Locate every Plasmodium falciparum-infected red blood cell.
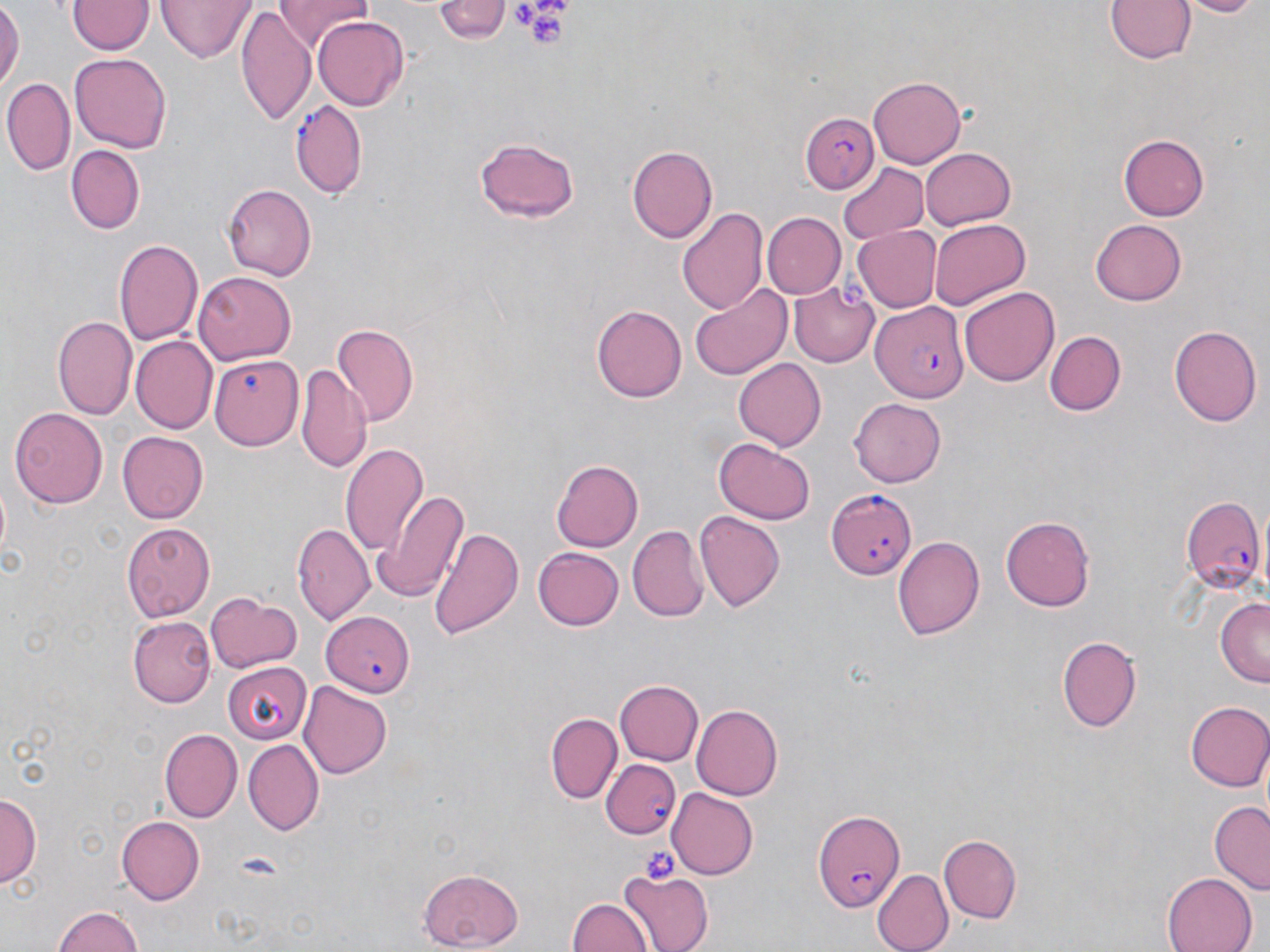
Approximate bounding boxes as (x1,y1)-(x2,y2) corner pairs in pixels.
Plasmodium falciparum-infected red blood cells: (291,99)-(367,198), (801,112)-(877,193), (869,300)-(966,407), (825,487)-(916,578), (1181,495)-(1266,592), (322,609)-(414,698), (601,760)-(681,839), (810,805)-(908,911).

Summary:
  - Uninfected red blood cell locations: (0,0)-(22,92), (158,0)-(255,63), (278,0)-(374,47), (432,0)-(511,43), (1105,0)-(1196,67), (1174,0)-(1264,17), (69,1)-(151,56), (236,8)-(313,124), (311,16)-(409,111), (70,53)-(172,152), (865,75)-(966,169), (4,79)-(75,173), (1120,134)-(1211,221), (476,135)-(581,224), (626,143)-(717,241), (66,145)-(146,233), (920,147)-(1018,230), (837,162)-(928,242), (222,183)-(314,279), (677,205)-(769,316), (761,213)-(844,298), (929,219)-(1030,311), (1089,219)-(1186,306), (853,226)-(940,311), (115,237)-(205,346), (194,270)-(297,362), (789,284)-(878,366), (690,285)-(793,379), (959,287)-(1059,386), (592,304)-(687,403), (52,315)-(137,421), (330,325)-(417,426), (1169,325)-(1261,428), (1044,330)-(1126,416), (131,335)-(218,432), (209,354)-(304,452), (735,358)-(828,450), (297,365)-(372,475), (849,397)-(948,486), (9,408)-(107,508), (117,430)-(209,521), (715,438)-(814,524), (341,446)-(429,558), (552,460)-(642,553), (374,487)-(468,602), (694,511)-(783,612), (1002,515)-(1098,610), (123,522)-(216,621), (293,524)-(375,625), (428,524)-(524,640), (629,526)-(708,622), (893,535)-(986,639), (533,544)-(624,629), (204,591)-(300,673), (1217,599)-(1269,687), (129,617)-(214,707), (1058,636)-(1142,732), (222,660)-(310,742), (299,679)-(392,778), (613,679)-(703,766), (1185,700)-(1270,791), (691,704)-(782,801), (546,712)-(622,803), (159,727)-(241,822), (242,738)-(322,834), (667,787)-(758,879), (0,791)-(41,884), (1209,803)-(1270,891), (115,816)-(205,903), (941,834)-(1022,921), (417,867)-(524,949), (871,868)-(953,952), (616,870)-(714,951), (1161,871)-(1258,951), (568,897)-(654,951), (52,906)-(148,952)
  - Platelet locations: (516,1)-(571,49), (638,844)-(680,885)
  - Slide-level diagnosis: Plasmodium falciparum
  - Stain: May-Grünwald-Giemsa
  - Magnification: 1000x
  - Modality: optical microscopy
  - Field of view: one of a larger specimen
  - Image size: 1270×952 pixels
  - Preparation: thin blood smear